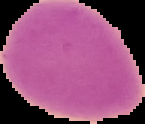

Summary:
  - Preparation: thin blood smear
  - Image type: segmented cell region on a black background
  - Result: negative for Plasmodium parasites
  - Image size: 145×124 pixels